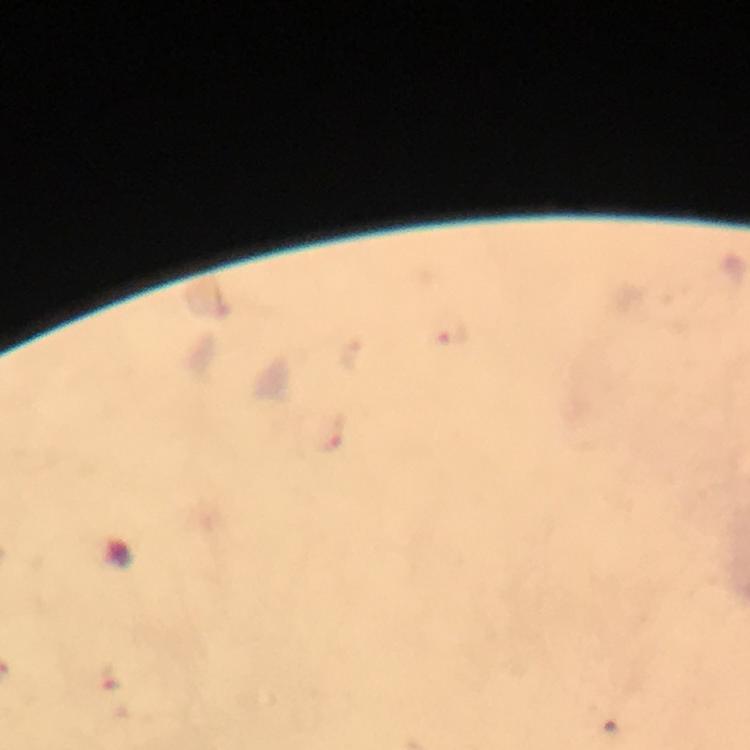

Approximate centers as [x, y] in pixels. Plasmodium parasite locations: [456, 334], [332, 436]. Image is 750×750 pixels. Thick blood smear. Immersion oil was used. A crop from one field of view. Smartphone photograph taken through a microscope. 100x magnification. Giemsa-stained preparation. From a diagnostic examination for malaria.